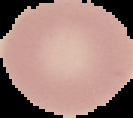
From a thin blood film. Cell region segmented out of the field of view; the surrounding area is masked to black. Result: negative for Plasmodium parasites. Image is 133×118 pixels.